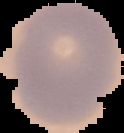

From a thin blood film. Image is 124×133 pixels. Result: no Plasmodium parasites detected. Cell region segmented out of the field of view; the surrounding area is masked to black.